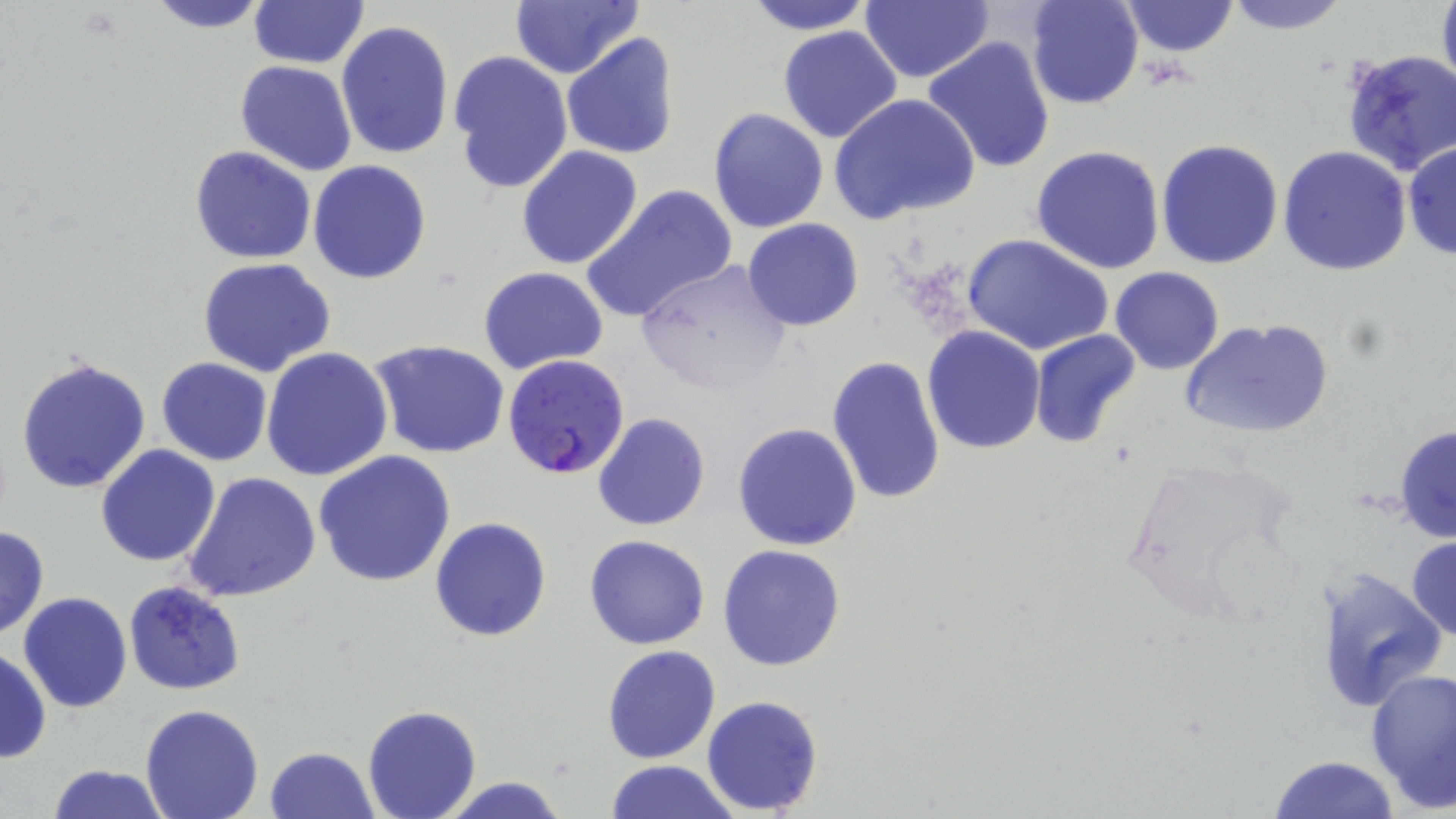
slide-level diagnosis = Plasmodium falciparum
stain = May-Grünwald-Giemsa
Plasmodium falciparum-infected red blood cell locations = approximate bounding boxes as [x1, y1, x2, y2] in pixels: [504, 354, 631, 481]
field of view = single
preparation = thin blood film
modality = optical microscopy
magnification = 1000x
image size = 1456×819 pixels
uninfected red blood cell locations = approximate bounding boxes as [x1, y1, x2, y2] in pixels: [144, 0, 276, 32], [248, 0, 368, 68], [508, 0, 644, 80], [741, 0, 875, 35], [1025, 0, 1143, 110], [1120, 0, 1238, 57], [1222, 0, 1351, 34], [1435, 0, 1456, 101], [860, 2, 993, 84], [336, 20, 453, 161], [778, 27, 904, 144], [561, 32, 679, 160], [764, 32, 940, 228], [921, 37, 1056, 175], [1337, 48, 1456, 176], [447, 50, 575, 197], [235, 61, 358, 176], [829, 93, 979, 227], [707, 108, 829, 233], [1156, 138, 1285, 269], [1403, 143, 1456, 260], [515, 145, 644, 270], [1031, 145, 1166, 275], [188, 146, 317, 264], [1277, 147, 1413, 277], [308, 160, 432, 283], [581, 182, 736, 323], [742, 219, 864, 331], [962, 234, 1116, 356], [197, 257, 336, 376], [633, 257, 796, 395], [477, 266, 609, 374], [1109, 266, 1225, 375], [1179, 316, 1333, 441], [921, 326, 1046, 454], [1028, 329, 1140, 449], [369, 338, 510, 458], [261, 347, 393, 483], [16, 355, 151, 493], [828, 355, 947, 506], [156, 357, 272, 466], [592, 412, 709, 531], [732, 422, 863, 552], [1394, 423, 1456, 545], [95, 445, 221, 567], [313, 451, 456, 587], [1117, 452, 1306, 630], [181, 472, 322, 602], [430, 516, 553, 642], [0, 524, 49, 640], [584, 534, 710, 650], [1406, 536, 1456, 644], [718, 544, 846, 671], [1313, 566, 1447, 712], [123, 581, 246, 696], [19, 592, 132, 712], [602, 645, 721, 765], [0, 646, 50, 763], [1364, 667, 1455, 812], [700, 694, 824, 815], [141, 705, 266, 819], [362, 705, 483, 819], [266, 746, 377, 819], [1266, 755, 1401, 819], [607, 761, 735, 818], [46, 764, 170, 819], [435, 774, 571, 819]